Assess this cell for malaria.
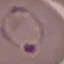
It is parasitized.

Giemsa-stained preparation. Automatically extracted cell patch, resized to 64 × 64 pixels. Photographed with a smartphone camera at the microscope eyepiece. Thin blood film.